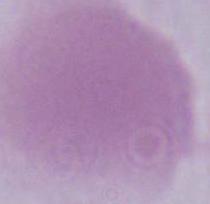
identification = Plasmodium
modality = photomicrograph
magnification = 400x or 1000x